Locate every uninfected red blood cell.
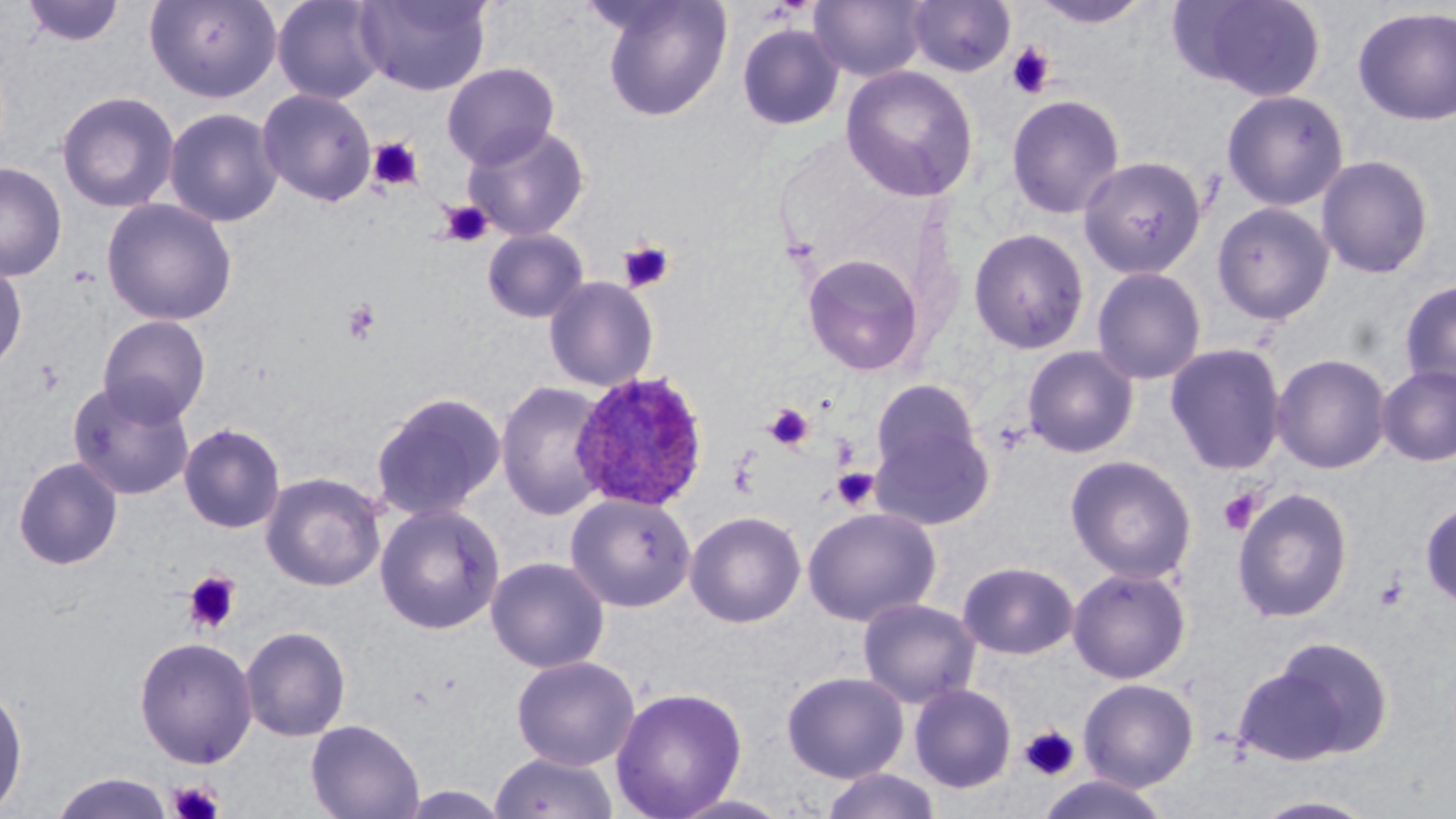

Approximate bounding boxes as (x1,y1)-(x2,y2) corner pairs in pixels.
Uninfected red blood cells: (20,0)-(127,47), (144,0)-(282,103), (271,0)-(388,104), (354,0)-(492,96), (597,0)-(733,121), (809,0)-(929,82), (907,0)-(1016,77), (1027,0)-(1155,29), (1171,0)-(1328,101), (1352,6)-(1456,126), (736,23)-(845,131), (442,63)-(559,168), (840,64)-(979,202), (256,88)-(378,207), (1221,89)-(1349,211), (56,91)-(180,213), (1006,94)-(1125,219), (164,107)-(284,228), (462,123)-(589,241), (1316,154)-(1434,278), (1078,155)-(1207,278), (0,162)-(67,281), (100,198)-(238,326), (1211,201)-(1335,325), (968,227)-(1090,354), (481,228)-(590,323), (801,252)-(925,376), (0,260)-(27,377), (1091,266)-(1208,385), (543,276)-(659,392), (1398,278)-(1456,394), (97,315)-(211,426), (1164,342)-(1288,475), (1021,345)-(1139,458), (1270,353)-(1392,474), (1376,364)-(1456,467), (67,379)-(196,500), (870,379)-(984,484), (496,380)-(612,520), (370,391)-(506,521), (871,418)-(996,532), (178,423)-(286,533), (1065,454)-(1198,584), (12,456)-(123,570), (260,472)-(386,591), (1231,487)-(1354,623), (565,493)-(696,613), (1419,499)-(1456,609), (374,504)-(505,634), (802,506)-(942,626), (685,510)-(806,628), (485,556)-(610,673), (957,560)-(1079,660), (1068,567)-(1192,684), (858,597)-(982,709), (240,625)-(351,742), (133,636)-(257,769), (1243,637)-(1393,764), (511,655)-(640,771), (781,670)-(909,783), (1079,678)-(1199,791), (0,679)-(28,817), (909,683)-(1017,794), (610,686)-(747,819), (305,718)-(424,819), (490,750)-(620,819), (819,768)-(943,819), (50,772)-(174,819), (1035,773)-(1171,818), (397,785)-(511,818), (668,793)-(796,819), (1251,794)-(1382,818).

Summary:
  - Platelet locations: (1006,42)-(1055,99), (367,137)-(424,192), (440,200)-(492,246), (618,240)-(676,293), (342,298)-(382,345), (763,402)-(816,452), (831,467)-(879,510), (1218,489)-(1261,534), (183,570)-(242,634), (1375,570)-(1410,611), (1018,725)-(1080,781), (168,780)-(225,819)
  - Plasmodium ovale-infected red blood cell locations: (569,369)-(710,512)
  - Slide-level diagnosis: Plasmodium ovale
  - Image size: 1456×819 pixels
  - Modality: light microscopy
  - Magnification: 1000x
  - Preparation: thin blood smear
  - Field of view: one of a larger specimen
  - Stain: May-Grünwald-Giemsa